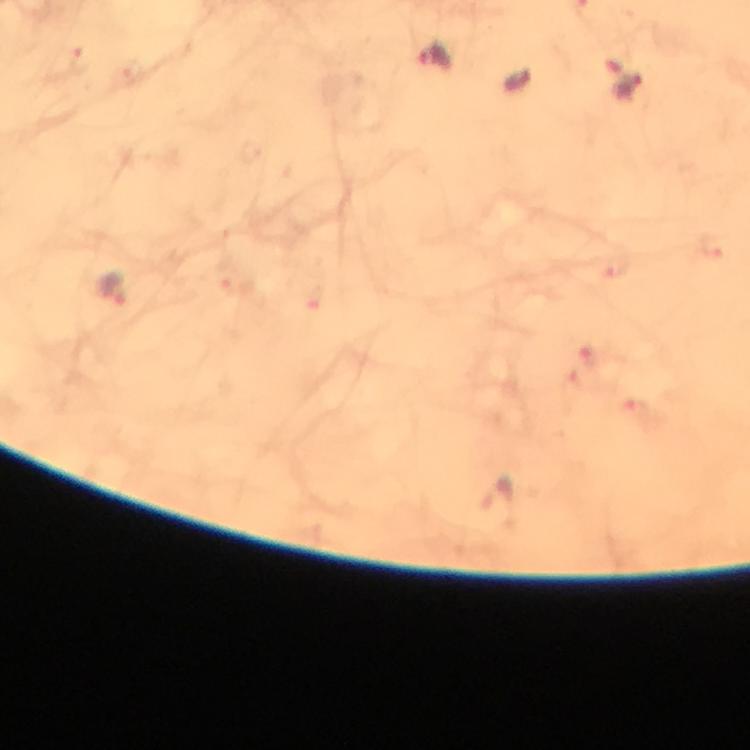
immersion oil = used
malaria parasite locations = approximate object centers, in pixels from the top-left corner: (x=434, y=56), (x=629, y=85), (x=111, y=287)
cropped from = a single field of view
context = from a malaria diagnostic workup
capture = smartphone camera through the microscope
image size = 750×750 pixels
preparation = thick blood film
stain = Giemsa
magnification = 100x